Identify the parasite.
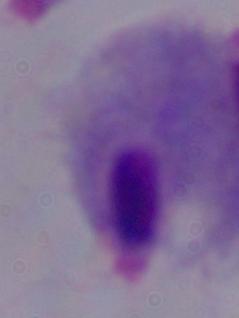
This is a trichomonad.

magnification = 1000x
modality = photomicrograph